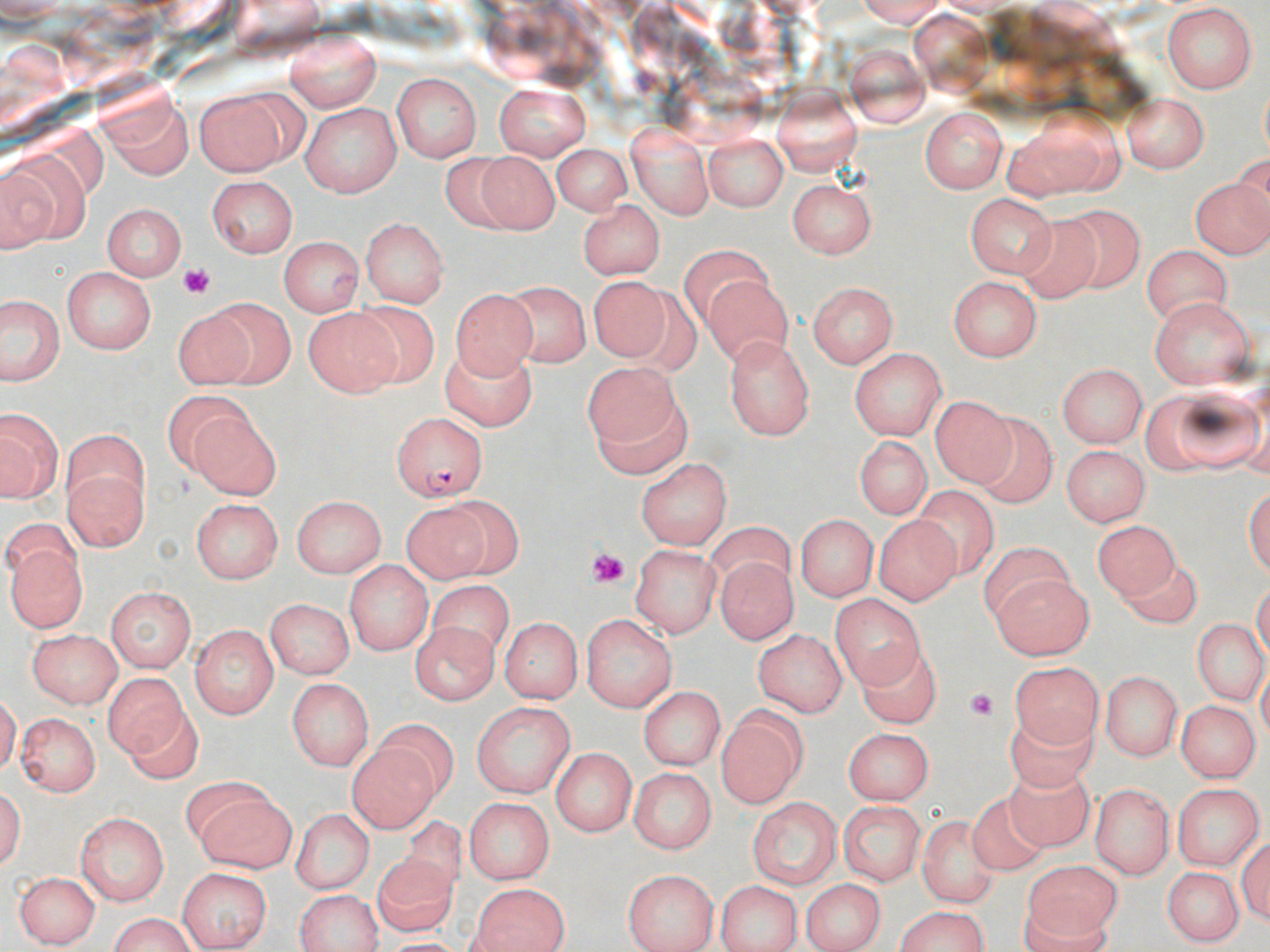 Approximate bounding boxes as [x1, y1, x2, y2] in pixels. Uninfected red blood cell locations: [1162, 5, 1259, 95], [287, 29, 380, 111], [848, 46, 932, 125], [392, 72, 483, 161], [493, 79, 595, 160], [772, 87, 861, 172], [194, 88, 293, 179], [1120, 92, 1208, 171], [106, 100, 189, 183], [300, 102, 401, 197], [920, 107, 1009, 194], [1004, 112, 1120, 199], [627, 122, 714, 219], [704, 132, 788, 212], [548, 143, 636, 215], [437, 148, 528, 236], [474, 151, 557, 232], [2, 158, 71, 252], [1191, 169, 1270, 259], [207, 177, 301, 258], [789, 178, 877, 261], [966, 191, 1055, 279], [577, 198, 667, 278], [105, 202, 188, 280], [1069, 207, 1140, 285], [1016, 212, 1095, 298], [360, 216, 450, 307], [278, 237, 363, 320], [1141, 241, 1234, 323], [680, 243, 777, 326], [64, 268, 157, 354], [700, 274, 790, 374], [949, 276, 1043, 361], [585, 277, 672, 362], [505, 281, 587, 370], [807, 281, 897, 370], [450, 285, 539, 375], [207, 294, 294, 389], [1151, 295, 1256, 389], [0, 298, 70, 384], [355, 301, 435, 385], [172, 303, 258, 389], [300, 304, 401, 396], [722, 331, 816, 439], [440, 341, 537, 434], [852, 347, 944, 439], [582, 361, 679, 448], [1058, 361, 1149, 446], [1168, 382, 1261, 473], [930, 390, 1013, 486], [596, 394, 690, 479], [180, 409, 278, 496], [4, 410, 58, 500], [973, 411, 1057, 503], [852, 436, 935, 518], [1061, 445, 1147, 527], [63, 453, 149, 551], [639, 455, 733, 548], [910, 483, 995, 579], [294, 493, 387, 577], [448, 497, 523, 578], [194, 498, 284, 582], [404, 505, 488, 584], [794, 515, 876, 603], [876, 515, 956, 604], [1093, 515, 1183, 605], [709, 524, 796, 589], [7, 538, 85, 632], [978, 542, 1073, 622], [630, 543, 719, 637], [718, 558, 796, 647], [343, 561, 430, 653], [1121, 563, 1206, 629], [994, 572, 1091, 659], [427, 582, 505, 668], [105, 589, 197, 674], [831, 592, 923, 685], [263, 599, 353, 679], [580, 613, 677, 712], [499, 616, 580, 705], [1183, 616, 1260, 705], [408, 623, 501, 704], [191, 624, 278, 718], [28, 627, 120, 710], [753, 630, 844, 715], [858, 640, 942, 722], [1008, 660, 1100, 751], [1103, 669, 1184, 760], [104, 677, 188, 763], [287, 678, 371, 772], [641, 685, 724, 769], [1178, 699, 1256, 782], [126, 701, 204, 785], [472, 701, 576, 799], [717, 703, 808, 808], [367, 714, 458, 801], [16, 715, 99, 798], [1008, 716, 1100, 795], [843, 727, 934, 804], [350, 741, 441, 837], [550, 748, 637, 834], [627, 766, 719, 852], [1002, 772, 1096, 852], [177, 779, 274, 844], [1173, 781, 1264, 869], [1089, 785, 1170, 879], [966, 790, 1051, 875], [194, 796, 297, 867], [462, 797, 555, 883], [747, 798, 845, 886], [837, 801, 927, 883], [402, 807, 480, 887], [75, 810, 171, 905], [294, 813, 371, 894], [921, 815, 994, 905], [368, 856, 458, 935], [1024, 859, 1121, 943], [1160, 865, 1245, 946], [172, 866, 273, 946], [11, 870, 97, 946], [623, 870, 717, 952], [800, 876, 882, 952], [717, 880, 802, 952], [468, 882, 569, 952], [294, 889, 386, 951], [891, 908, 992, 952], [102, 916, 199, 950]. Plasmodium falciparum-infected red blood cell locations: [392, 412, 486, 502]. Platelet locations: [174, 260, 216, 296], [585, 538, 626, 588], [968, 684, 996, 721]. Slide-level diagnosis: Plasmodium falciparum. May-Grünwald-Giemsa-stained preparation. Optical microscopy. One field of a larger specimen. Thin blood film. 1000x magnification. Image is 1270×952 pixels.